Comment on the morphology of the red blood cells.
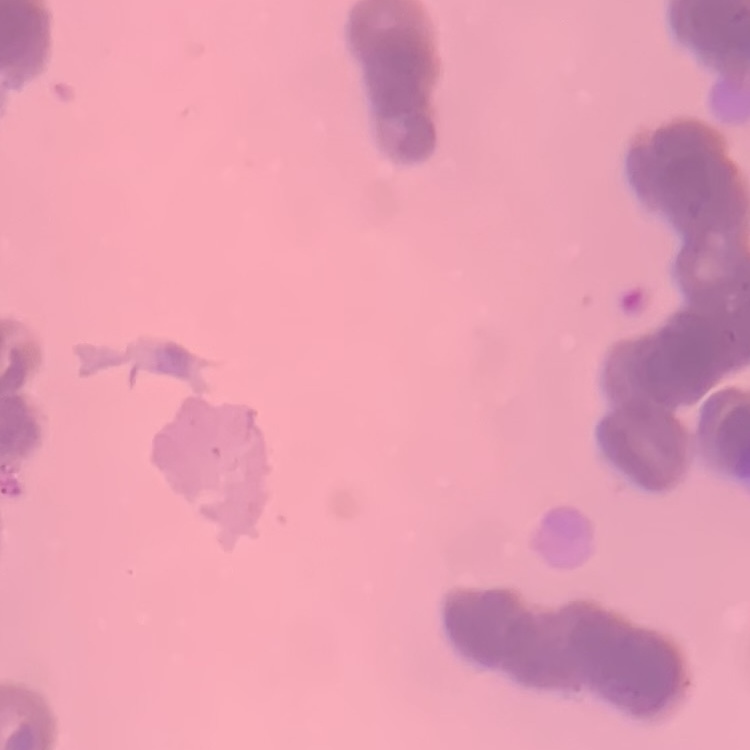
They show rouleaux formation.

Summary:
  - Stain: Field's or Giemsa
  - Image type: square crop of a larger photomicrograph
  - Preparation: thin blood film